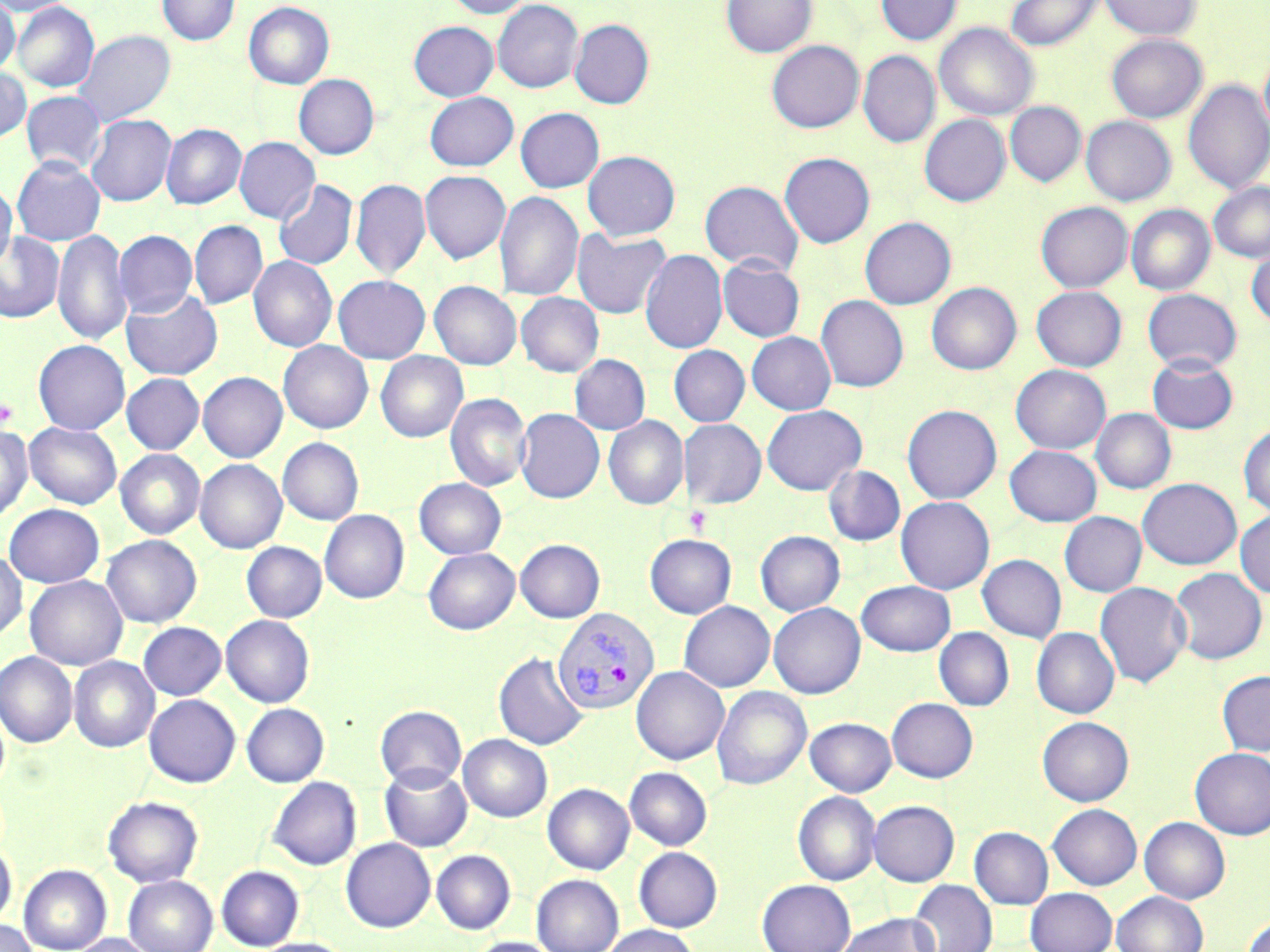

Summary:
  - Coordinate format: approximate bounding boxes as (x1,y1)-(x2,y2) corner pairs in pixels
  - Platelet locations: (0,397)-(17,429), (683,506)-(712,537)
  - Plasmodium vivax-infected red blood cell locations: (553,607)-(659,715)
  - Uninfected red blood cell locations: (0,0)-(76,17), (157,0)-(240,46), (444,0)-(533,18), (722,0)-(817,58), (876,0)-(962,45), (1005,0)-(1103,51), (1099,0)-(1201,40), (0,1)-(20,75), (492,1)-(583,93), (12,2)-(99,93), (243,2)-(334,89), (570,19)-(654,109), (409,21)-(498,101), (934,23)-(1038,120), (74,30)-(175,127), (1106,34)-(1207,122), (767,41)-(863,132), (858,51)-(940,147), (1260,51)-(1270,139), (0,67)-(31,144), (293,74)-(379,159), (1184,79)-(1270,195), (21,91)-(106,174), (424,92)-(518,171), (1005,102)-(1085,187), (516,108)-(605,193), (86,114)-(176,207), (919,115)-(1010,206), (1081,116)-(1175,205), (161,124)-(246,210), (234,137)-(320,224), (582,151)-(680,241), (779,152)-(875,248), (12,156)-(105,246), (420,170)-(511,264), (351,178)-(431,282), (0,179)-(17,272), (273,179)-(357,271), (700,180)-(804,276), (1209,182)-(1270,263), (495,191)-(583,303), (1036,202)-(1132,292), (1126,204)-(1215,295), (860,217)-(956,309), (189,221)-(268,309), (53,228)-(132,348), (572,229)-(671,319), (115,230)-(197,318), (0,231)-(64,323), (640,249)-(727,355), (1247,250)-(1270,327), (248,255)-(337,353), (717,258)-(805,342), (333,276)-(430,364), (429,281)-(522,370), (927,283)-(1021,375), (1031,286)-(1127,371), (121,288)-(222,380), (1143,289)-(1241,373), (516,292)-(603,377), (816,295)-(908,392), (747,332)-(836,415), (33,340)-(130,435), (278,341)-(373,434), (669,345)-(750,427), (376,352)-(468,442), (570,354)-(650,435), (1147,355)-(1239,435), (1010,364)-(1110,453), (198,372)-(287,463), (121,374)-(205,454), (445,393)-(532,492), (762,405)-(866,495), (902,405)-(1002,504), (1091,408)-(1176,494), (516,409)-(605,503), (603,416)-(688,510), (679,419)-(766,509), (24,422)-(122,510), (1238,424)-(1270,517), (0,425)-(33,524), (278,438)-(364,525), (1004,444)-(1101,526), (115,449)-(205,539), (195,459)-(287,554), (824,465)-(906,546), (414,478)-(506,559), (1138,478)-(1242,570), (896,496)-(995,594), (3,504)-(105,588), (320,509)-(409,604), (1235,509)-(1270,598), (1059,511)-(1147,597), (755,531)-(845,616), (645,534)-(736,618), (101,535)-(202,628), (515,539)-(605,622), (241,542)-(327,623), (423,547)-(520,635), (0,551)-(27,641), (977,554)-(1066,643), (1169,567)-(1267,664), (24,575)-(128,671), (856,580)-(956,656), (1096,581)-(1193,689), (678,601)-(775,692), (768,602)-(865,699), (221,615)-(314,707), (138,622)-(226,701), (1032,627)-(1119,719), (934,628)-(1014,711), (0,651)-(77,748), (494,651)-(588,751), (69,656)-(159,752), (631,666)-(729,765), (1217,671)-(1270,756), (712,686)-(811,790), (144,695)-(240,787), (887,698)-(978,783), (241,703)-(329,787), (375,705)-(467,790), (1038,716)-(1134,806), (805,717)-(896,796), (458,734)-(552,822), (1190,748)-(1270,839), (380,764)-(472,852), (625,767)-(712,850), (267,776)-(362,870), (542,783)-(634,874), (793,791)-(880,886), (103,795)-(203,887), (868,800)-(959,886), (1047,803)-(1141,890), (1140,817)-(1230,903), (969,826)-(1054,909), (341,838)-(435,932), (0,842)-(17,928), (634,847)-(722,932), (431,850)-(516,934), (18,864)-(112,952), (216,865)-(304,950), (532,874)-(623,952), (123,875)-(218,952), (757,879)-(856,952), (909,880)-(997,952), (1026,887)-(1117,952), (1112,891)-(1208,952), (837,913)-(940,952), (1242,913)-(1270,952), (0,919)-(38,952), (599,924)-(701,952), (71,933)-(157,952), (466,936)-(563,952), (253,937)-(353,952)
  - Slide-level diagnosis: Plasmodium vivax
  - Modality: light microscopy
  - Field of view: single
  - Preparation: thin blood smear
  - Stain: May-Grünwald-Giemsa
  - Magnification: 1000x
  - Image size: 1270×952 pixels